Locate every blood parasite and identify its species.
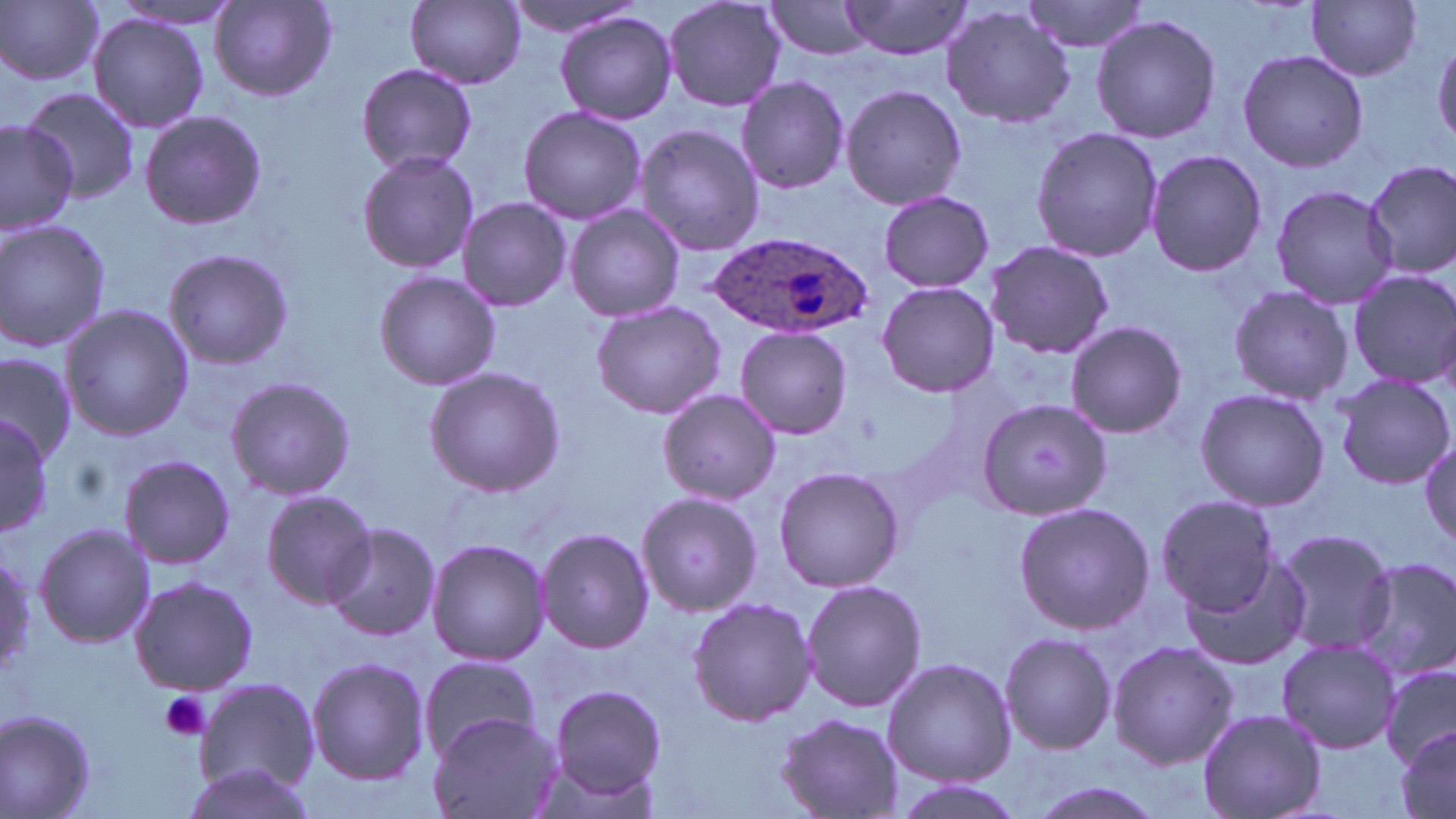

Approximate bounding boxes as (x1,y1)-(x2,y2) corner pairs in pixels.
Plasmodium ovale-infected red blood cells: (708,231)-(872,343).
No Plasmodium falciparum, Plasmodium malariae, Plasmodium vivax, Babesia divergens, or Trypanosoma brucei observed.

Summary:
  - Platelet locations: (159,690)-(211,741)
  - Uninfected red blood cell locations: (502,0)-(644,40), (663,0)-(787,113), (763,0)-(879,59), (837,0)-(973,61), (1022,0)-(1150,55), (0,1)-(105,85), (406,1)-(527,88), (107,2)-(244,29), (1308,2)-(1422,82), (210,3)-(336,101), (940,6)-(1076,128), (557,12)-(678,125), (88,15)-(209,134), (1091,15)-(1221,142), (1432,37)-(1455,151), (1235,49)-(1369,173), (356,64)-(477,173), (736,75)-(849,193), (839,84)-(966,210), (22,86)-(140,204), (518,105)-(646,225), (139,108)-(265,231), (0,118)-(80,234), (634,125)-(765,255), (1030,126)-(1164,264), (1144,149)-(1268,279), (356,150)-(479,274), (1364,159)-(1456,279), (1270,184)-(1398,309), (877,190)-(994,293), (458,197)-(573,313), (565,204)-(685,322), (0,219)-(112,355), (983,240)-(1113,358), (164,249)-(297,369), (1345,268)-(1456,388), (375,270)-(500,390), (877,280)-(1000,397), (1226,284)-(1354,405), (591,300)-(725,420), (61,304)-(192,441), (1064,320)-(1188,439), (735,326)-(852,441), (0,348)-(77,461), (424,367)-(564,498), (1332,373)-(1456,489), (225,375)-(356,500), (657,388)-(780,504), (1194,388)-(1329,511), (976,396)-(1117,520), (0,411)-(54,541), (1420,438)-(1455,550), (117,455)-(236,570), (773,465)-(905,592), (260,489)-(375,608), (638,492)-(764,616), (1154,496)-(1280,615), (1013,500)-(1153,635), (322,523)-(441,642), (33,524)-(154,648), (536,528)-(655,653), (1273,529)-(1395,655), (426,538)-(552,667), (0,551)-(35,682), (1185,557)-(1311,674), (1349,557)-(1456,686), (128,576)-(259,695), (801,577)-(924,713), (686,596)-(815,726), (1000,633)-(1117,755), (1275,637)-(1399,753), (1106,639)-(1238,769), (306,657)-(430,786), (416,657)-(542,755), (883,657)-(1016,786), (1383,662)-(1456,769), (194,677)-(320,796), (545,682)-(669,807), (1197,707)-(1327,819), (1,709)-(99,819), (427,710)-(556,819), (774,712)-(906,817), (1393,727)-(1455,819), (178,762)-(319,818), (894,779)-(1025,819), (1022,779)-(1170,819)
  - Slide-level diagnosis: Plasmodium ovale
  - Magnification: 1000x
  - Stain: May-Grünwald-Giemsa
  - Preparation: thin blood smear
  - Image size: 1456×819 pixels
  - Field of view: single
  - Modality: light microscopy